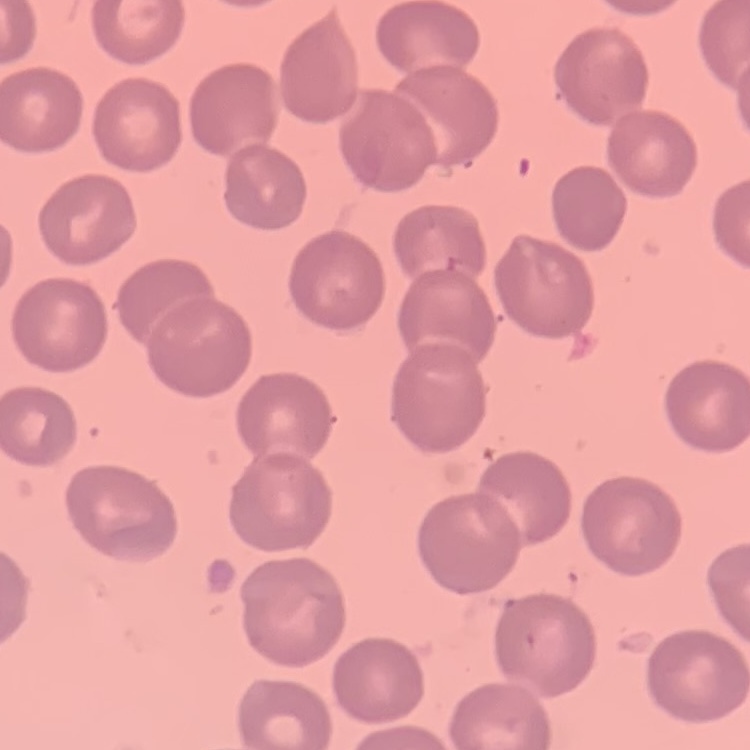 The erythrocytes show no rouleaux formation. Field's or Giemsa stain. One tile cut from a larger photomicrograph. Thin blood film.